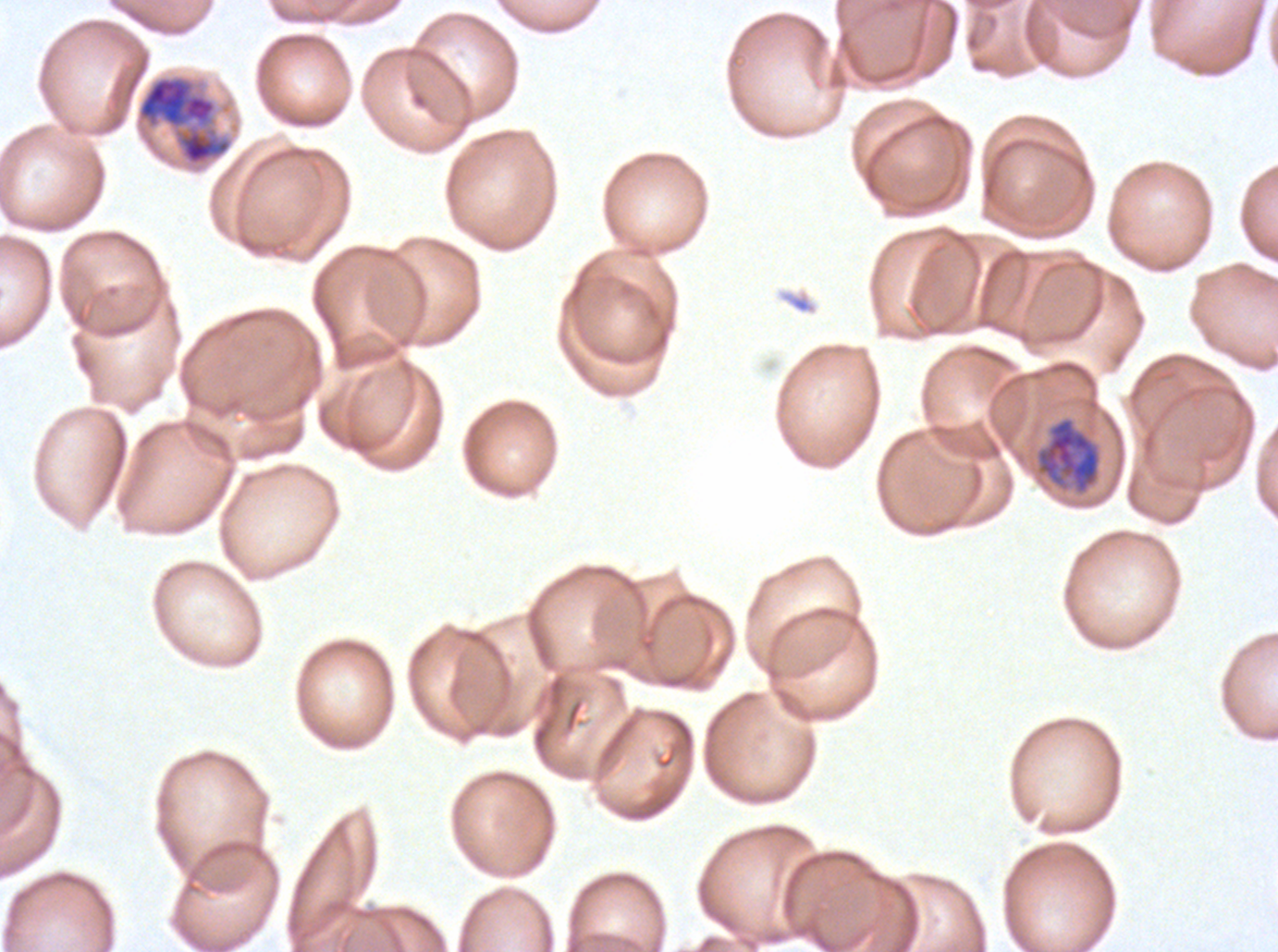
Approximate bounding boxes as {x1, y1, x2, y2} in pixels. Early schizont locations: {136, 74, 233, 167}. Late trophozoite locations: {1035, 416, 1101, 494}. Life-cycle stages observed: late trophozoite, early schizont. Thin blood smear. P. falciparum cultured ex vivo for 24 to 48 hours, from a patient in The Gambia. Image is 1278×952 pixels. A sub-image separated from a larger composite. Giemsa stain.